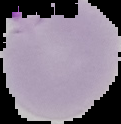
Summary:
  - Preparation: thin blood smear
  - Image size: 121×124 pixels
  - Image type: segmented cell region on a black background
  - Result: malaria parasites detected